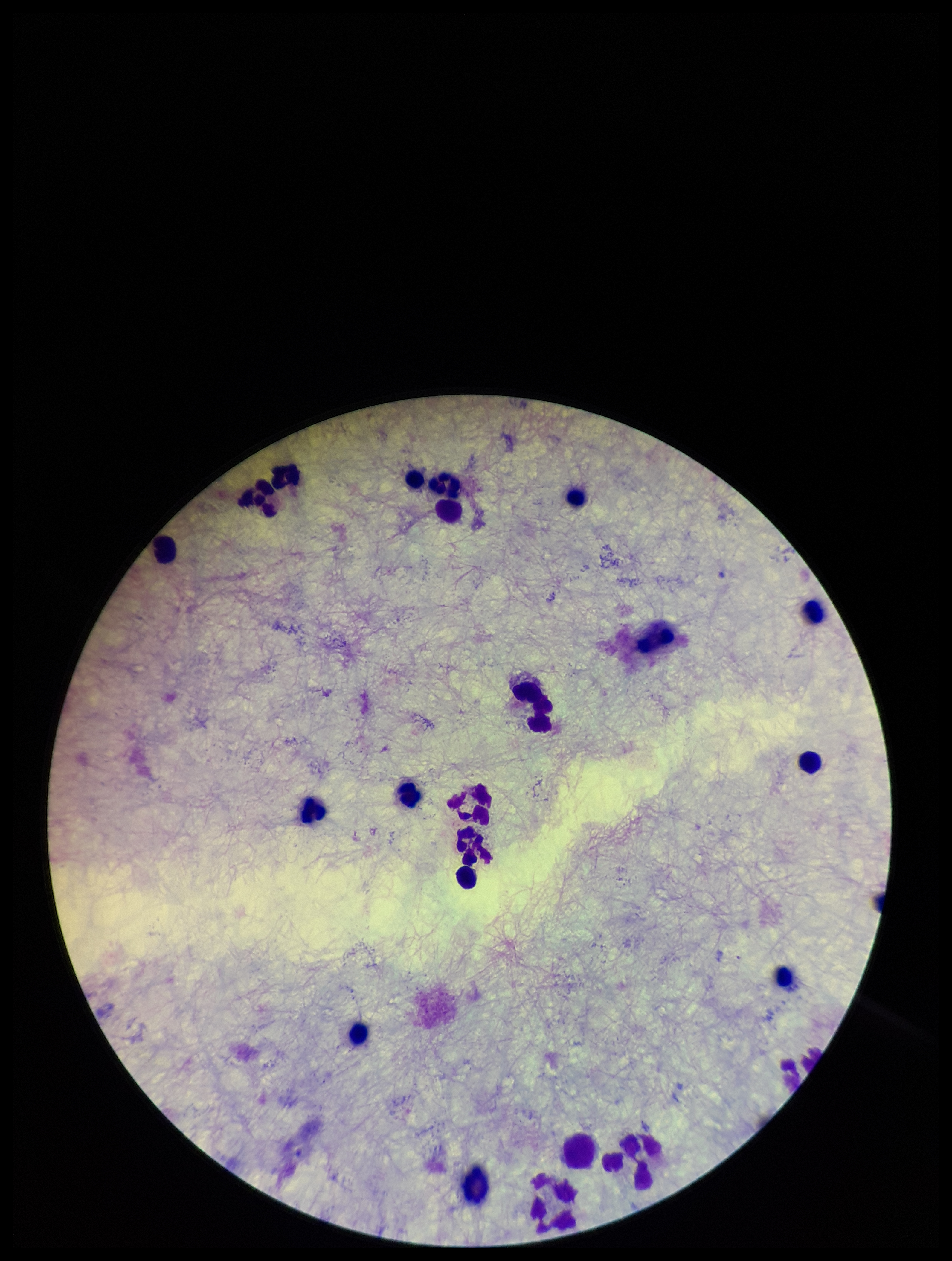

Plasmodium parasites: none seen. Leukocyte count: 21. Giemsa stain. Smartphone photograph taken through the eyepiece of a microscope. Single field of view. Parasite count: 0. Patient malaria status: negative. Image is 952×1261 pixels. Preparation: thick smear.